Classify this cell by malaria status.
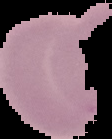
Uninfected.

Summary:
  - Preparation: thin blood film
  - Image type: segmented cell region with the area outside set to black
  - Image size: 112×139 pixels